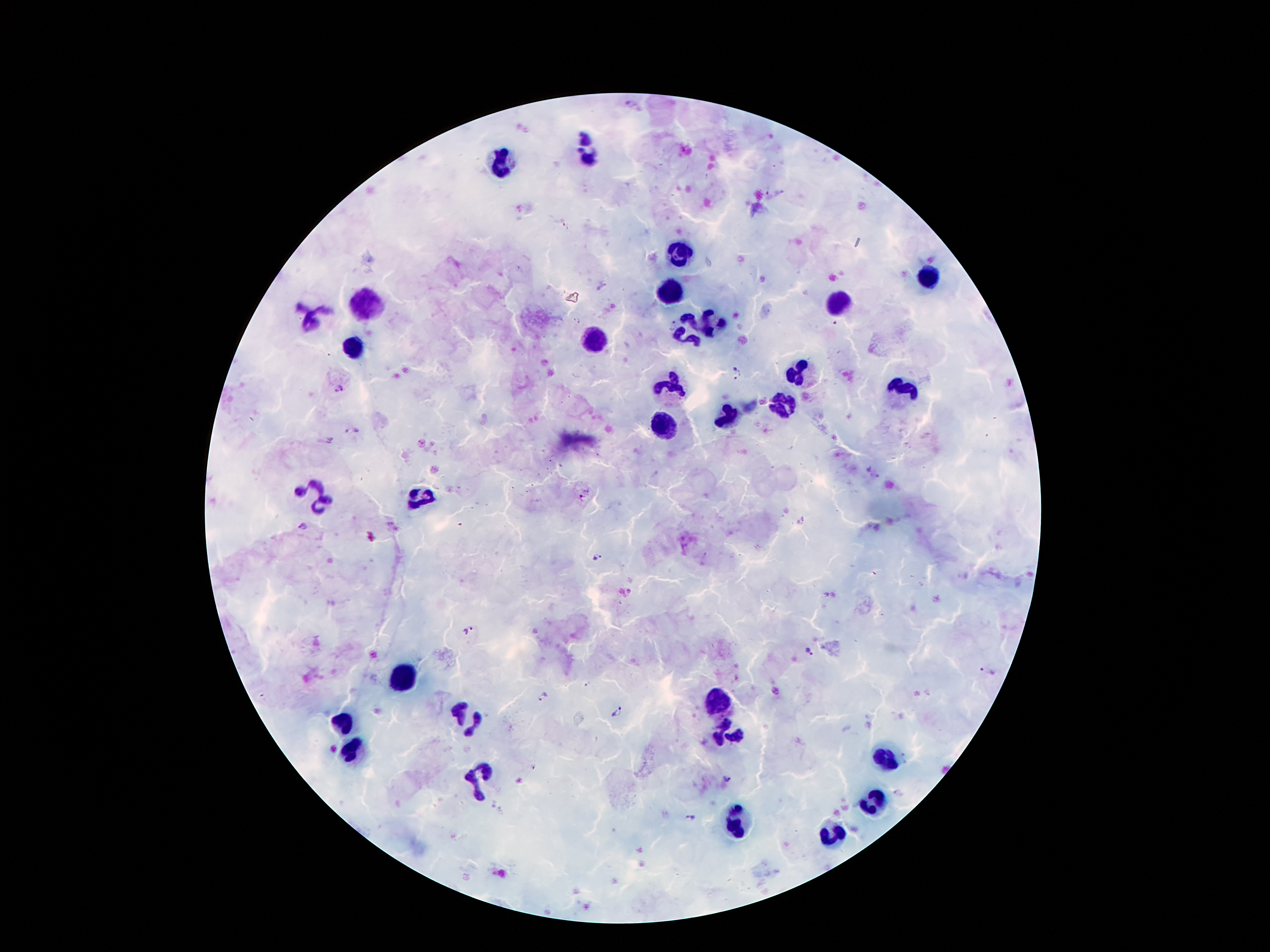
Approximate object centers, in pixels from the top-left corner. Plasmodium parasite locations: (x=672, y=324), (x=737, y=373), (x=337, y=388), (x=353, y=432), (x=585, y=494), (x=304, y=526), (x=598, y=557), (x=469, y=631), (x=810, y=652), (x=989, y=672), (x=545, y=695), (x=617, y=712), (x=727, y=779), (x=898, y=792), (x=689, y=817). Leukocyte locations: (x=588, y=145), (x=501, y=164), (x=677, y=253), (x=929, y=275), (x=669, y=294), (x=837, y=302), (x=366, y=304), (x=311, y=315), (x=705, y=321), (x=596, y=342), (x=686, y=342), (x=354, y=346), (x=801, y=375), (x=671, y=388), (x=902, y=391), (x=786, y=402), (x=729, y=419), (x=663, y=427), (x=315, y=492), (x=417, y=499), (x=409, y=676), (x=720, y=701), (x=465, y=717), (x=342, y=724), (x=728, y=733), (x=354, y=749), (x=888, y=758), (x=474, y=779), (x=874, y=800), (x=740, y=822), (x=831, y=833). Patient malaria status: positive for Plasmodium falciparum. Photographed through the microscope eyepiece with a smartphone camera. Thick blood film. 100x magnification. Giemsa-stained preparation. Image is 1270×952 pixels. One field from this slide.